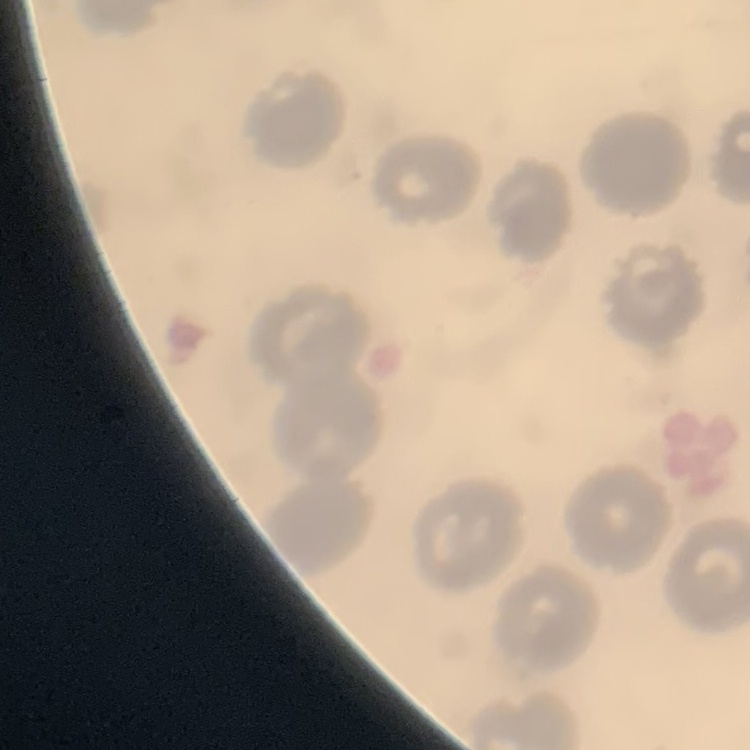
Summary:
  - Erythrocyte morphology: no rouleaux formation
  - Preparation: thin blood smear
  - Stain: Field's or Giemsa
  - Image type: one tile cut from a larger photomicrograph